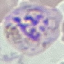

Summary:
  - Result: malaria parasites detected
  - Stain: Giemsa
  - Image type: cell patch, automatically extracted from a larger field of view and resized to 64 × 64 pixels
  - Preparation: thin blood smear
  - Capture: smartphone through the microscope eyepiece